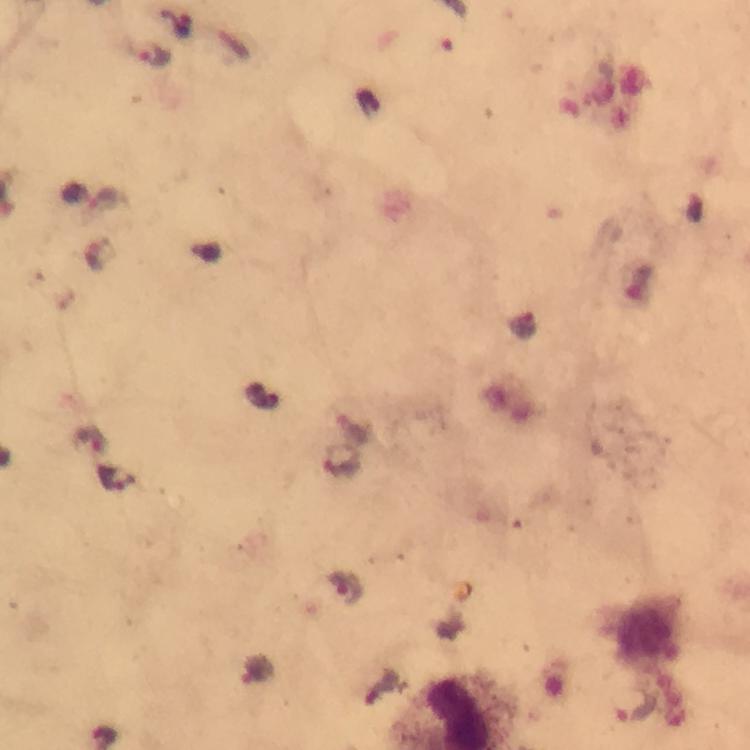 Approximate centers as (x, y) in pixels. Malaria parasite locations: (181, 24), (152, 54), (107, 201), (262, 394), (343, 464), (118, 479), (347, 587), (257, 671), (634, 707). Image is 750×750 pixels. 100x magnification. Giemsa stain. Thick smear. From a diagnostic examination for malaria. Smartphone photograph taken through a microscope. Immersion oil applied. A crop from one field of view.